Classify this cell by malaria status.
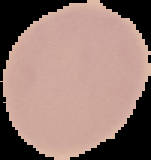
It is uninfected.

image size = 151×160 pixels
image type = segmented cell region on a black background
preparation = thin blood smear